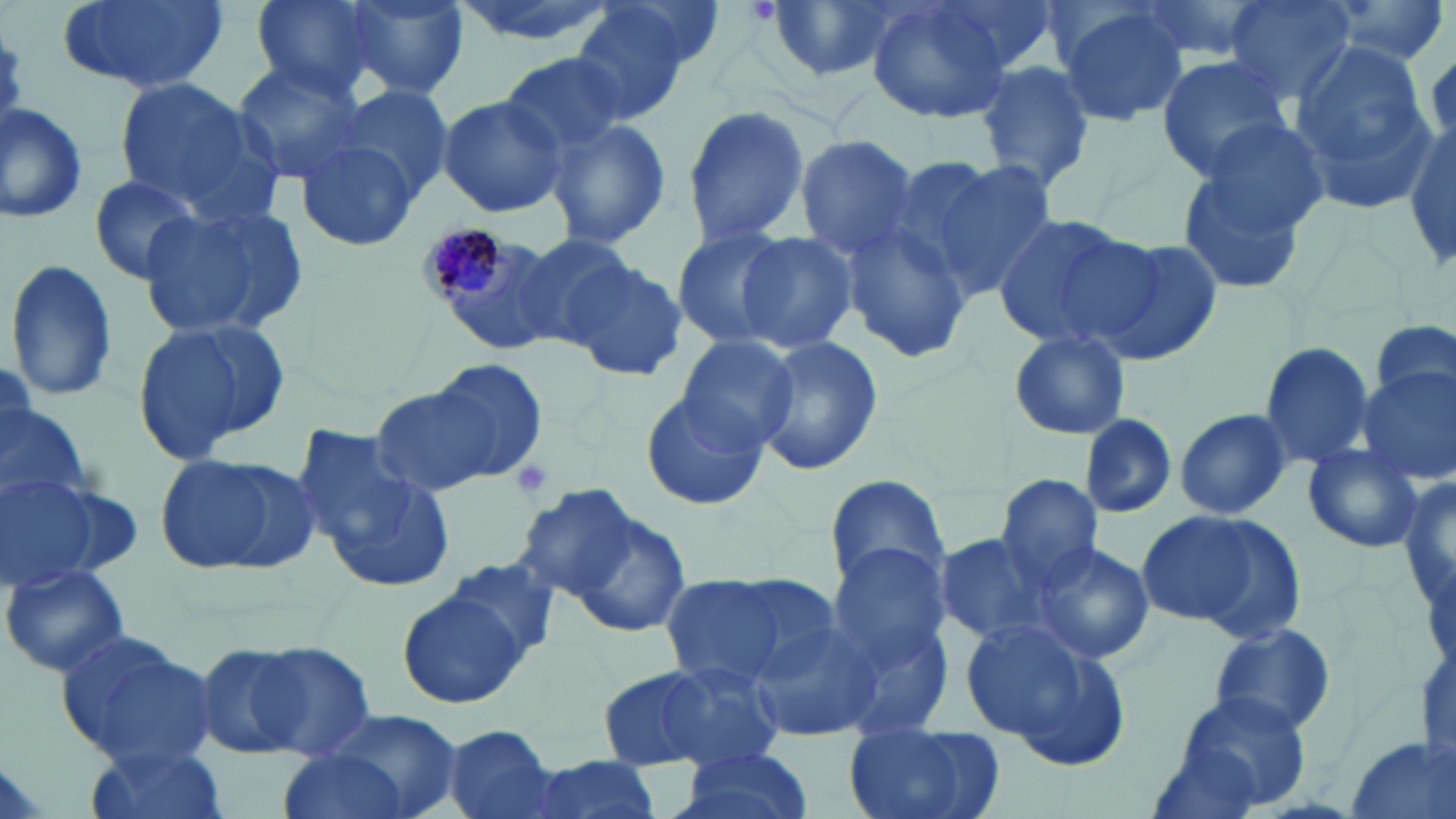

Summary:
  - Coordinate format: approximate bounding boxes as (x1, y1, x2, y2) in pixels
  - Plasmodium malariae-infected red blood cell locations: (419, 224, 523, 312)
  - Uninfected red blood cell locations: (53, 0, 230, 98), (249, 0, 378, 96), (342, 0, 468, 99), (763, 0, 897, 82), (865, 0, 1010, 126), (937, 0, 1074, 73), (1126, 0, 1272, 68), (1221, 0, 1356, 104), (1319, 0, 1451, 66), (1050, 2, 1189, 128), (570, 3, 708, 123), (1285, 35, 1436, 213), (498, 53, 630, 164), (1155, 55, 1294, 179), (231, 58, 368, 182), (974, 61, 1095, 192), (114, 76, 275, 217), (331, 84, 455, 203), (436, 93, 567, 219), (0, 100, 92, 226), (681, 100, 812, 249), (545, 116, 673, 253), (1405, 122, 1456, 272), (792, 135, 921, 261), (1174, 135, 1323, 297), (293, 138, 417, 255), (907, 154, 1060, 300), (83, 175, 207, 284), (138, 199, 309, 342), (990, 215, 1152, 355), (838, 222, 973, 363), (671, 227, 800, 351), (737, 230, 858, 353), (505, 231, 637, 353), (1086, 235, 1221, 368), (556, 247, 690, 378), (5, 257, 120, 405), (130, 314, 294, 462), (1370, 317, 1455, 413), (1006, 331, 1131, 441), (674, 335, 800, 454), (755, 337, 885, 476), (1259, 341, 1376, 468), (428, 359, 546, 477), (1357, 366, 1456, 486), (366, 380, 513, 495), (638, 388, 769, 512), (0, 406, 91, 509), (1174, 408, 1291, 521), (1078, 416, 1177, 518), (292, 428, 454, 590), (1301, 444, 1424, 553), (153, 450, 316, 576), (1401, 468, 1455, 618), (1, 469, 133, 587), (825, 472, 950, 596), (994, 474, 1102, 589), (516, 483, 643, 600), (554, 504, 694, 641), (1139, 508, 1301, 639), (933, 532, 1060, 646), (825, 539, 957, 679), (1033, 542, 1153, 663), (438, 552, 563, 668), (0, 561, 130, 678), (658, 573, 822, 688), (398, 587, 534, 709), (743, 614, 884, 739), (960, 618, 1133, 771), (1209, 621, 1339, 737), (54, 627, 219, 772), (244, 641, 376, 761), (194, 643, 307, 758), (635, 656, 789, 773), (596, 665, 724, 771), (1167, 689, 1311, 815), (319, 707, 461, 819), (440, 725, 559, 819), (843, 725, 1005, 819), (79, 738, 229, 819), (1343, 738, 1455, 819), (670, 747, 814, 819), (274, 748, 411, 819), (518, 754, 664, 819)
  - Platelet locations: (509, 458, 555, 503)
  - Slide-level diagnosis: Plasmodium malariae
  - Stain: May-Grünwald-Giemsa
  - Modality: optical microscopy
  - Preparation: thin blood smear
  - Image size: 1456×819 pixels
  - Magnification: 1000x
  - Field of view: one of a larger specimen